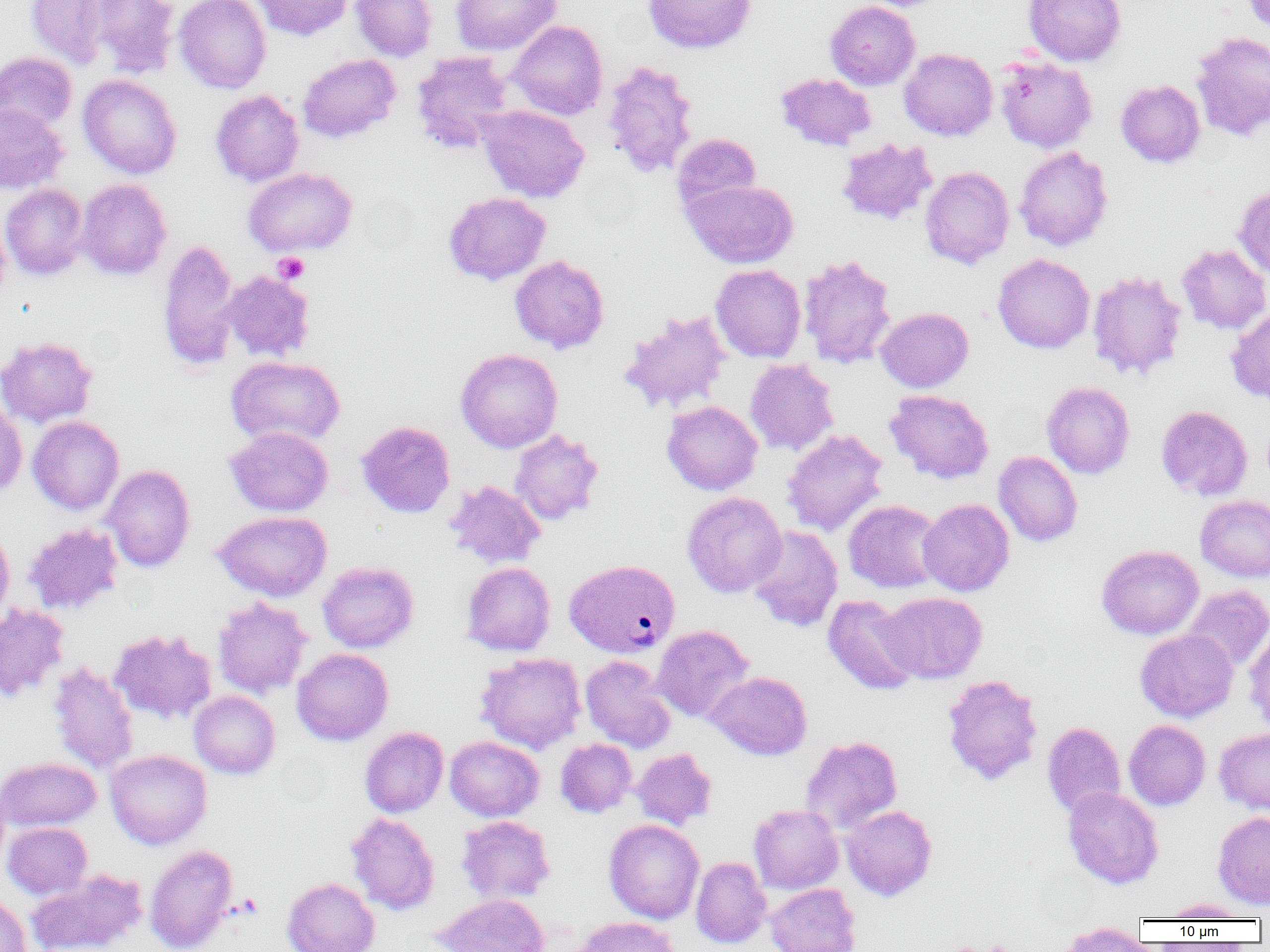 Approximate bounding boxes as (x1,y1)-(x2,y2) corner pairs in pixels. Plasmodium vivax-infected red blood cell locations: (564,562)-(680,660). Platelet locations: (273,252)-(310,284). Uninfected red blood cell locations: (25,0)-(118,69), (88,0)-(180,78), (174,0)-(272,93), (250,0)-(354,41), (351,0)-(437,62), (451,0)-(562,56), (643,0)-(756,54), (1023,0)-(1126,66), (1241,0)-(1270,34), (825,1)-(920,90), (507,20)-(608,120), (1191,32)-(1270,141), (899,48)-(998,141), (0,51)-(77,134), (412,51)-(514,154), (298,53)-(401,142), (995,55)-(1097,152), (602,60)-(699,178), (776,72)-(876,151), (78,74)-(182,179), (1116,79)-(1205,168), (210,89)-(305,187), (0,103)-(68,194), (477,105)-(590,203), (672,133)-(761,216), (836,137)-(937,226), (1014,146)-(1113,251), (920,166)-(1014,269), (242,167)-(357,256), (76,178)-(172,280), (682,178)-(799,269), (1233,182)-(1270,280), (0,184)-(90,280), (443,192)-(551,285), (0,215)-(11,305), (157,238)-(241,371), (1176,244)-(1270,334), (798,254)-(897,369), (993,254)-(1094,353), (510,255)-(609,354), (711,264)-(806,362), (1087,270)-(1187,380), (222,271)-(315,362), (876,307)-(973,392), (1226,308)-(1270,404), (618,310)-(733,415), (0,336)-(98,428), (455,348)-(563,453), (226,355)-(345,448), (745,358)-(839,456), (1042,381)-(1135,479), (884,389)-(994,484), (0,399)-(27,499), (662,401)-(762,495), (1155,405)-(1253,501), (27,416)-(124,515), (357,421)-(456,518), (225,426)-(333,516), (509,429)-(604,525), (781,429)-(888,537), (993,451)-(1083,546), (102,464)-(195,572), (444,480)-(545,569), (682,492)-(787,598), (1195,494)-(1270,582), (917,498)-(1014,596), (844,500)-(945,593), (213,510)-(332,602), (24,523)-(123,615), (0,525)-(14,627), (747,525)-(843,631), (1096,545)-(1203,639), (317,561)-(419,652), (462,562)-(555,656), (1183,585)-(1270,671), (876,591)-(987,684), (823,595)-(922,695), (212,597)-(311,698), (0,604)-(69,701), (652,625)-(754,723), (1244,628)-(1270,732), (109,629)-(217,725), (1135,629)-(1238,722), (292,648)-(393,745), (476,652)-(586,754), (580,656)-(676,753), (49,661)-(139,775), (706,671)-(812,760), (941,674)-(1043,785), (188,690)-(280,779), (1124,719)-(1211,810), (1042,722)-(1126,817), (360,727)-(448,817), (1214,727)-(1270,815), (444,736)-(544,821), (800,736)-(902,833), (555,739)-(637,817), (631,748)-(717,829), (105,749)-(212,849), (0,756)-(101,832), (0,782)-(10,874), (1063,786)-(1164,889), (749,804)-(844,895), (841,804)-(937,901), (1212,811)-(1270,909), (346,812)-(440,915), (456,815)-(555,904), (604,819)-(704,924), (3,822)-(92,899), (144,844)-(238,952), (691,857)-(771,949), (25,869)-(149,952), (282,877)-(379,952), (765,883)-(861,952), (434,893)-(549,952), (0,894)-(32,952), (1158,899)-(1253,921), (572,916)-(681,952), (1056,922)-(1149,951). Slide-level diagnosis: Plasmodium vivax. One field of a larger specimen. Thin blood smear. Light microscopy. Image is 1270×952 pixels. 1000x magnification.